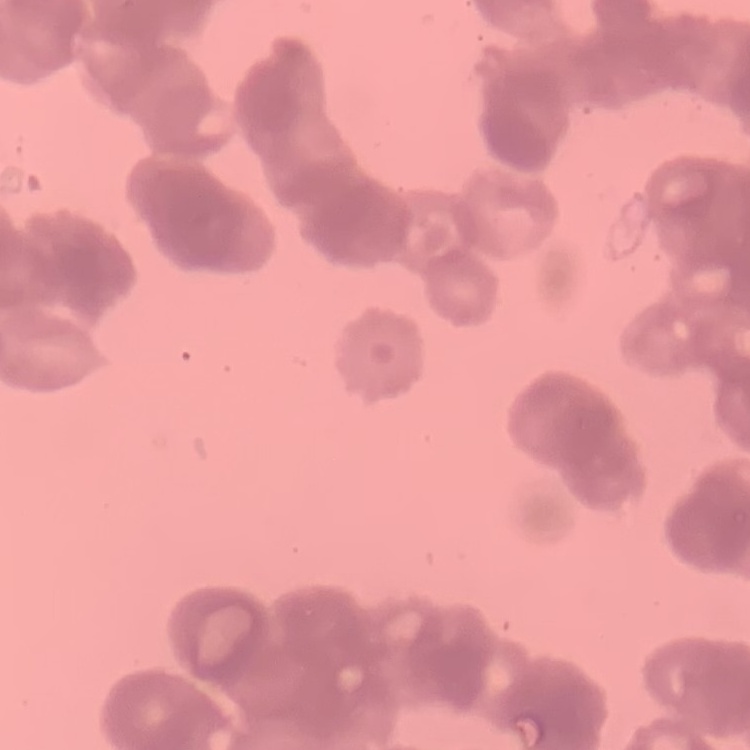
red blood cell morphology = rouleaux formation
stain = Field's or Giemsa
preparation = thin peripheral smear
image type = one tile cut from a larger photomicrograph